Identify the parasite.
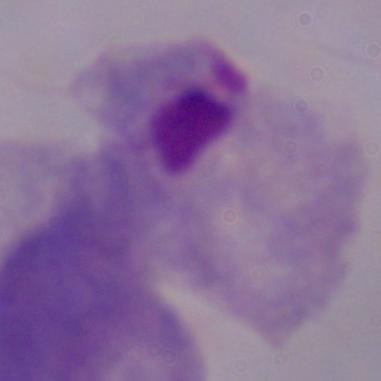
This is a trichomonad.

Summary:
  - Modality: photomicrograph
  - Magnification: 1000x